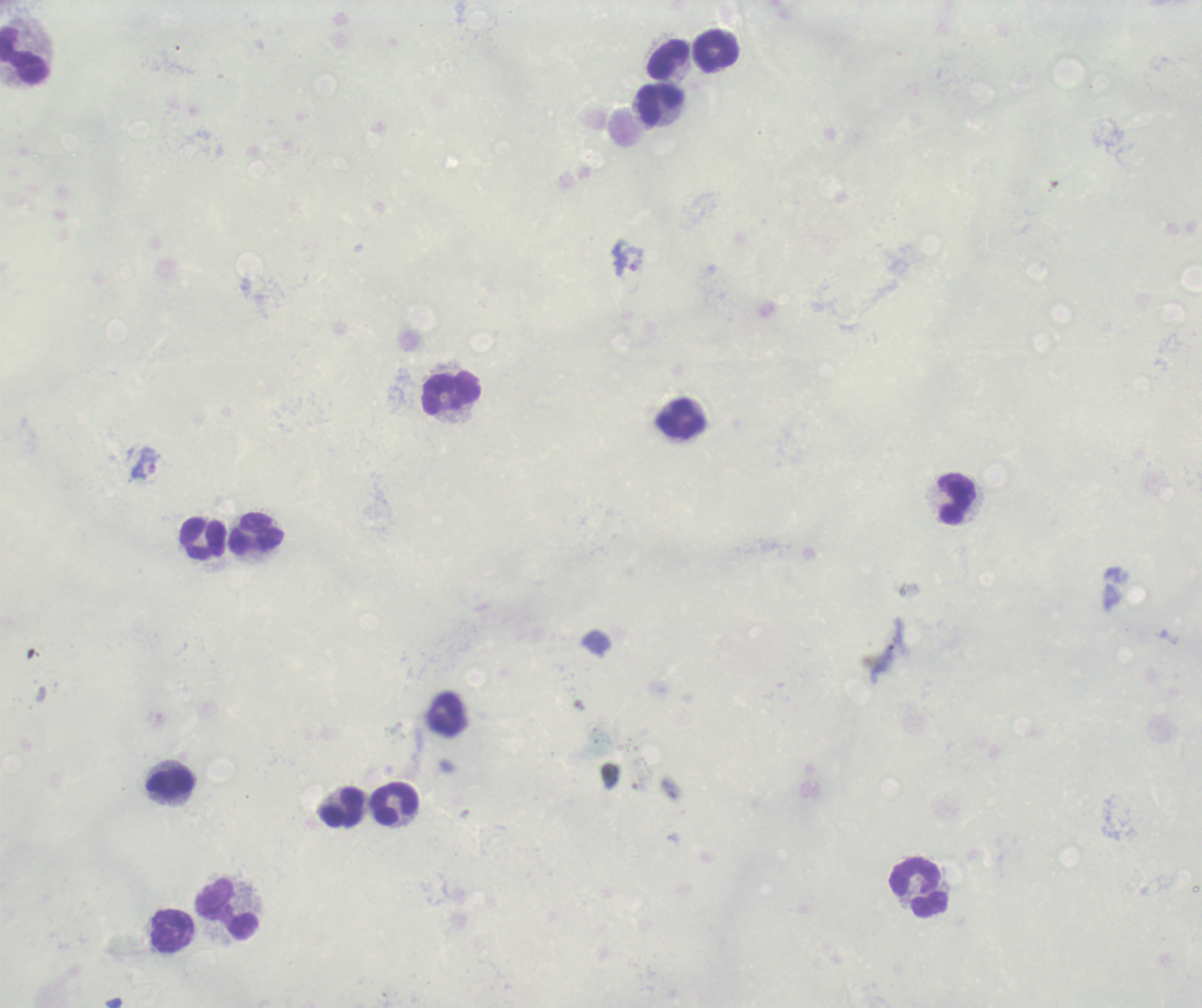 Approximate object centers, in pixels from the top-left corner. Leukocyte locations: (x=717, y=51), (x=25, y=55), (x=669, y=59), (x=662, y=106), (x=452, y=394), (x=681, y=420), (x=956, y=499), (x=257, y=534), (x=204, y=539), (x=447, y=714), (x=172, y=784), (x=396, y=805), (x=342, y=809), (x=920, y=887), (x=228, y=910), (x=173, y=930). Trophozoite locations: (x=629, y=260), (x=146, y=464). Previously used in an actual diagnosis. Thick blood smear. Background quality: unsatisfactory. Single field of view. Result: malaria parasites detected. Romanowsky stain. Image is 1202×1008 pixels. 100x magnification.